Name the parasite shown.
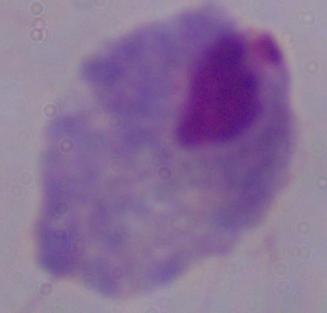
This is a trichomonad.

Summary:
  - Modality: micrograph
  - Magnification: 1000x